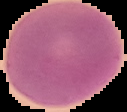

Image is 127×112 pixels. From a thin blood smear. The area outside the segmented cell region is set to black. Malaria status: uninfected.